Report the malaria status of this cell.
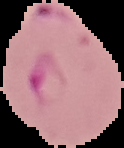
It is parasitized.

image_type: cell region segmented out of the field of view; surrounding area masked to black
image_size: 124×148 pixels
preparation: thin blood smear